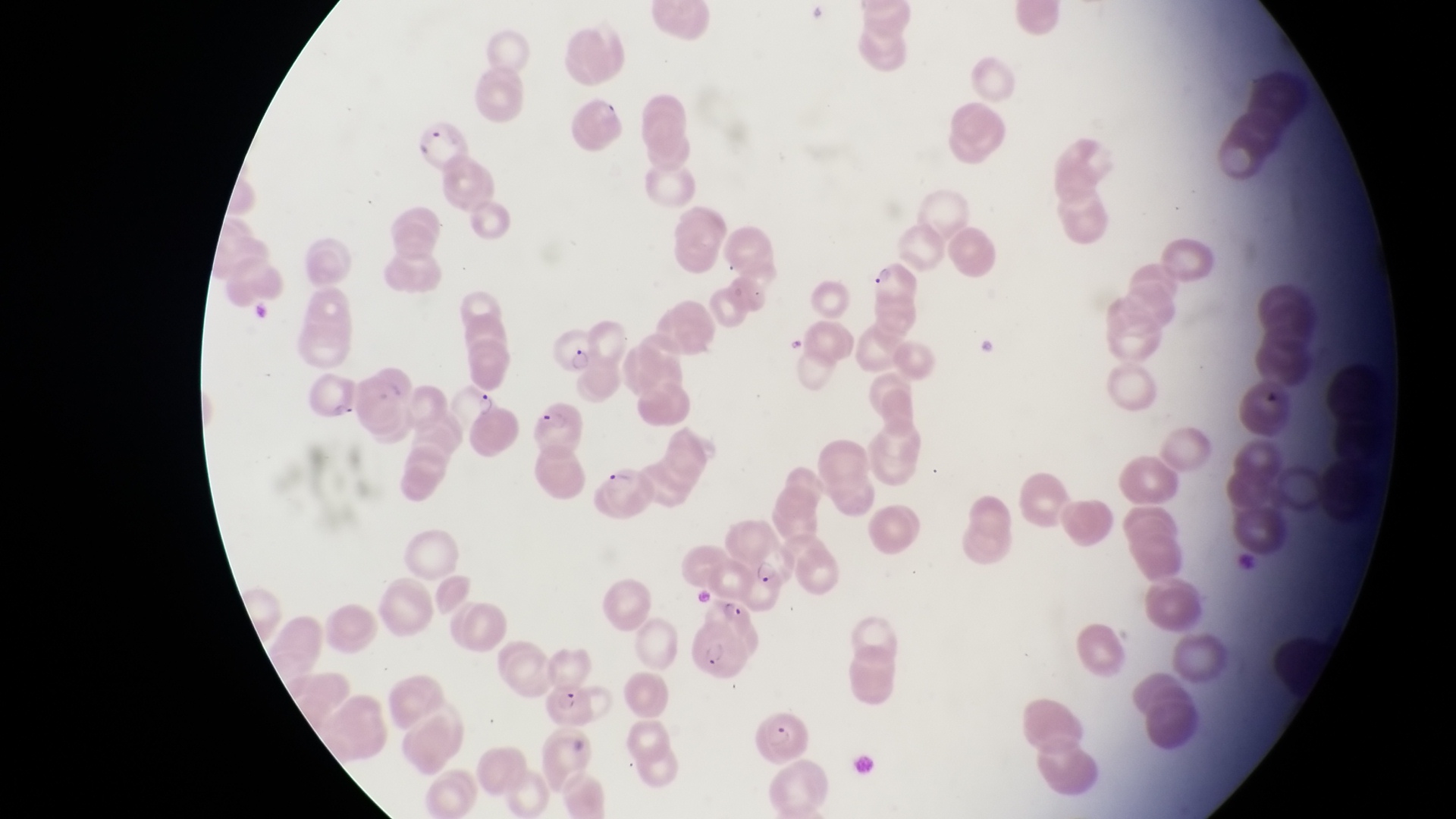
Approximate bounding boxes as {left, top, right, bottom} in pixels. Parasitised red blood cell locations: {416, 118, 469, 176}, {865, 257, 923, 302}, {547, 325, 605, 378}, {300, 366, 358, 425}, {453, 383, 509, 438}, {528, 394, 591, 453}, {594, 468, 657, 527}, {739, 548, 795, 617}, {687, 623, 753, 683}, {547, 680, 602, 735}, {752, 700, 821, 767}. Photographed through the eyepiece of an Olympus CX-23 microscope with a smartphone camera. Image is 1456×819 pixels. Thin blood film. Magnification of 1000x. Sample from Uganda. One field of view.